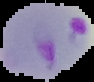

The area outside the segmented cell region is set to black. From a thin blood smear. Result: malaria parasites identified. Image is 94×82 pixels.